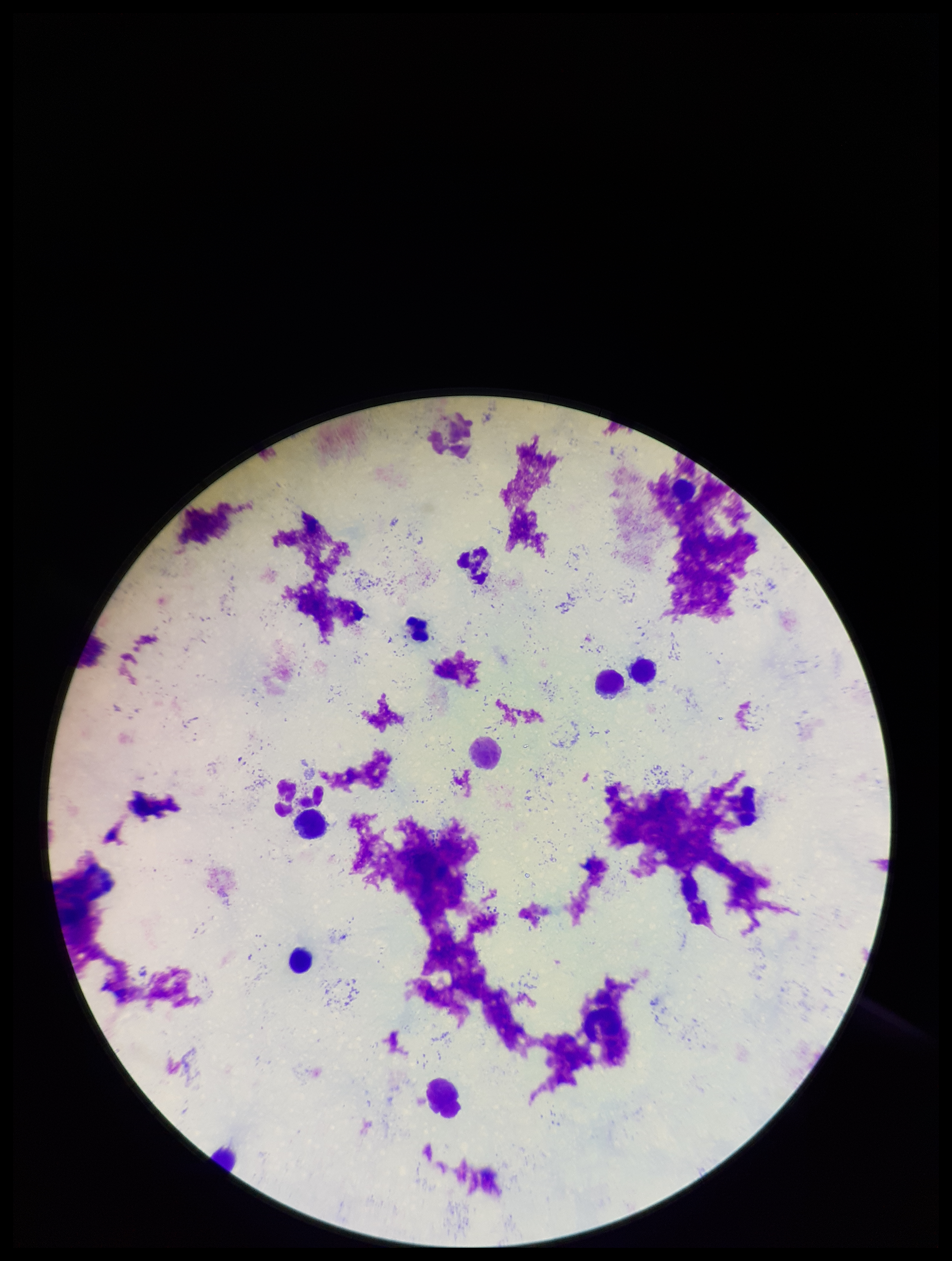

Parasite count: 0. Patient malaria status: negative. Plasmodium parasites: none seen. Single field of view. Preparation: thick smear. Image is 952×1261 pixels. Photographed through the microscope eyepiece with a smartphone camera. Giemsa stain. Leukocyte count: 8.